Report the malaria status of this cell.
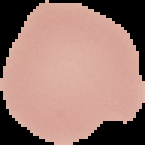
Uninfected.

image size = 145×145 pixels
image type = cell region segmented out of the field of view; surrounding area masked to black
preparation = thin blood film